Classify this cell by malaria status.
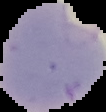

It is parasitized.

{
  "image_type": "segmented cell region on a black background",
  "image_size": "106×112 pixels",
  "preparation": "thin blood smear"
}